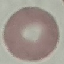
Result: no malaria parasites detected. Cell patch, automatically extracted from a larger field of view and resized to 64 × 64 pixels. Photographed with a smartphone camera at the microscope eyepiece. Giemsa stain. Thin blood smear.